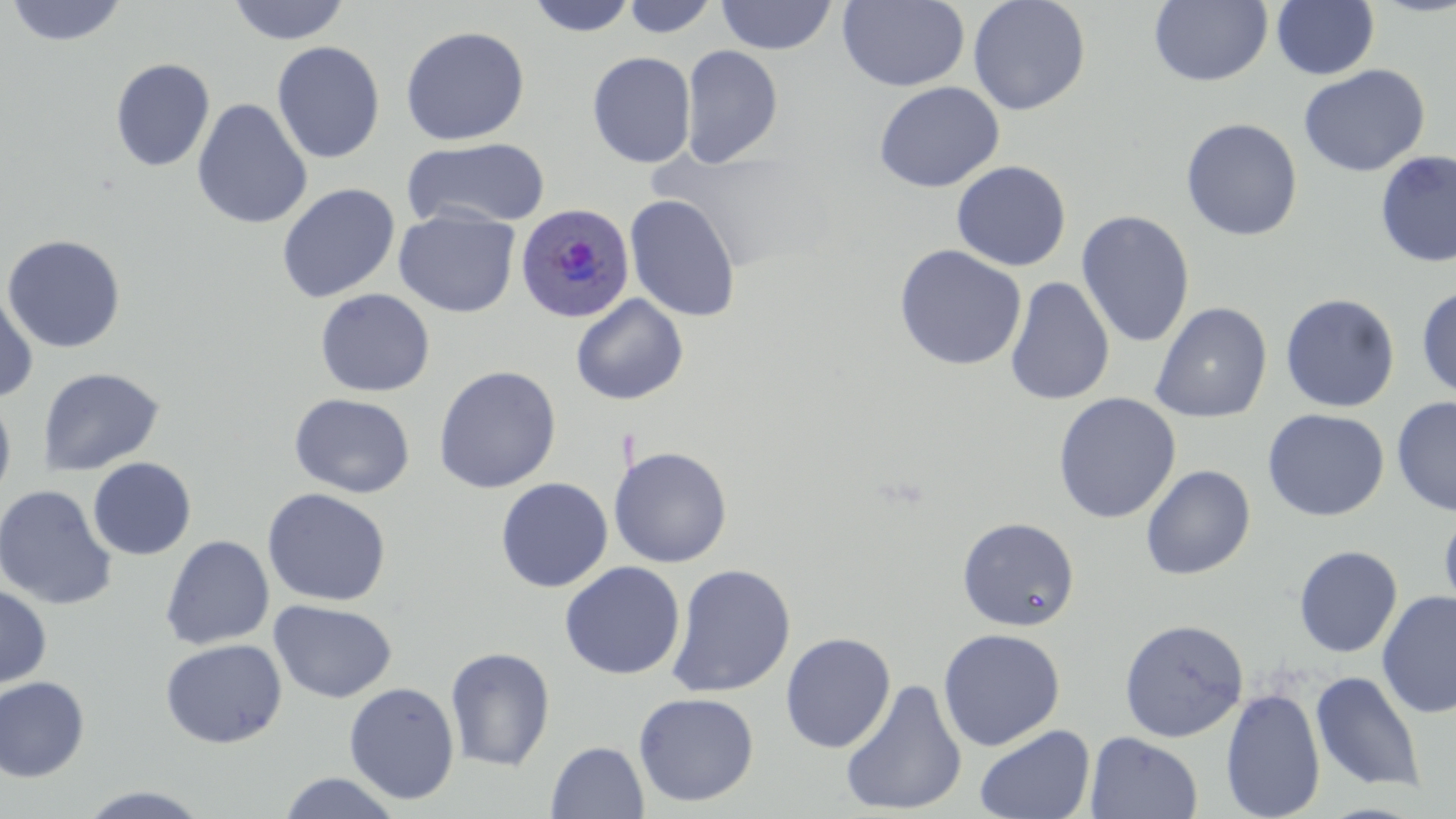
slide-level diagnosis = Plasmodium ovale
field of view = single
modality = light microscopy
image size = 1456×819 pixels
stain = May-Grünwald-Giemsa
magnification = 1000x
uninfected red blood cell locations = approximate bounding boxes as (x1, y1, x2, y2) in pixels: (4, 0, 129, 48), (227, 0, 349, 45), (525, 0, 639, 37), (619, 0, 720, 38), (714, 0, 838, 55), (838, 0, 969, 91), (967, 0, 1091, 116), (1271, 0, 1380, 80), (1148, 1, 1273, 87), (399, 25, 530, 146), (271, 41, 385, 164), (680, 44, 784, 168), (587, 51, 696, 168), (110, 58, 215, 172), (1298, 64, 1430, 177), (873, 81, 1004, 193), (192, 98, 312, 229), (1180, 117, 1303, 241), (401, 137, 551, 229), (653, 149, 835, 273), (1375, 150, 1456, 268), (951, 160, 1072, 271), (276, 183, 400, 303), (625, 194, 741, 322), (394, 208, 520, 318), (1076, 210, 1195, 348), (2, 234, 126, 353), (893, 244, 1027, 371), (1005, 276, 1115, 406), (0, 284, 38, 403), (1416, 286, 1456, 400), (314, 288, 435, 397), (1280, 293, 1400, 413), (570, 294, 689, 406), (1150, 301, 1272, 423), (433, 365, 561, 494), (37, 367, 164, 477), (1053, 392, 1181, 524), (289, 393, 415, 498), (0, 394, 16, 509), (1392, 396, 1456, 517), (1262, 408, 1389, 521), (609, 445, 732, 568), (87, 457, 196, 560), (1140, 464, 1256, 580), (495, 477, 613, 592), (0, 484, 118, 611), (262, 488, 391, 607), (1439, 505, 1456, 620), (957, 516, 1079, 631), (160, 535, 274, 649), (1293, 544, 1402, 658), (560, 561, 685, 680), (667, 563, 796, 698), (0, 585, 52, 689), (1377, 588, 1456, 719), (269, 598, 397, 703), (1119, 618, 1249, 742), (938, 627, 1065, 751), (780, 632, 896, 753), (160, 638, 287, 748), (444, 647, 556, 772), (1310, 670, 1426, 794), (0, 676, 90, 782), (840, 678, 967, 816), (344, 681, 460, 804), (1219, 686, 1326, 819), (633, 691, 759, 807), (974, 725, 1095, 819), (1084, 731, 1203, 819), (546, 741, 649, 819), (276, 771, 404, 819), (76, 786, 213, 818)
preparation = thin blood film
Plasmodium ovale-infected red blood cell locations = approximate bounding boxes as (x1, y1, x2, y2) in pixels: (514, 202, 635, 322)